Locate every Plasmodium parasite.
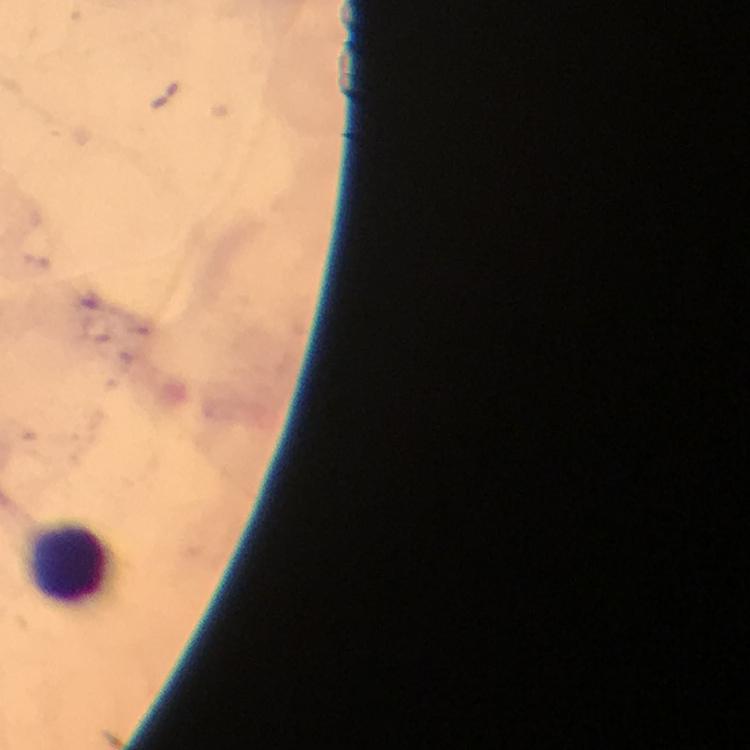
No Plasmodium parasites detected.

image_size: 750×750 pixels
leukocyte_locations: 'approximate centers as {x, y} in pixels: {68, 557}'
context: from a malaria diagnostic workup
cropped_from: a single field of view
immersion_oil: used
stain: Giemsa
magnification: 100x
preparation: thick smear
capture: smartphone mounted on the microscope